Give the preparation type.
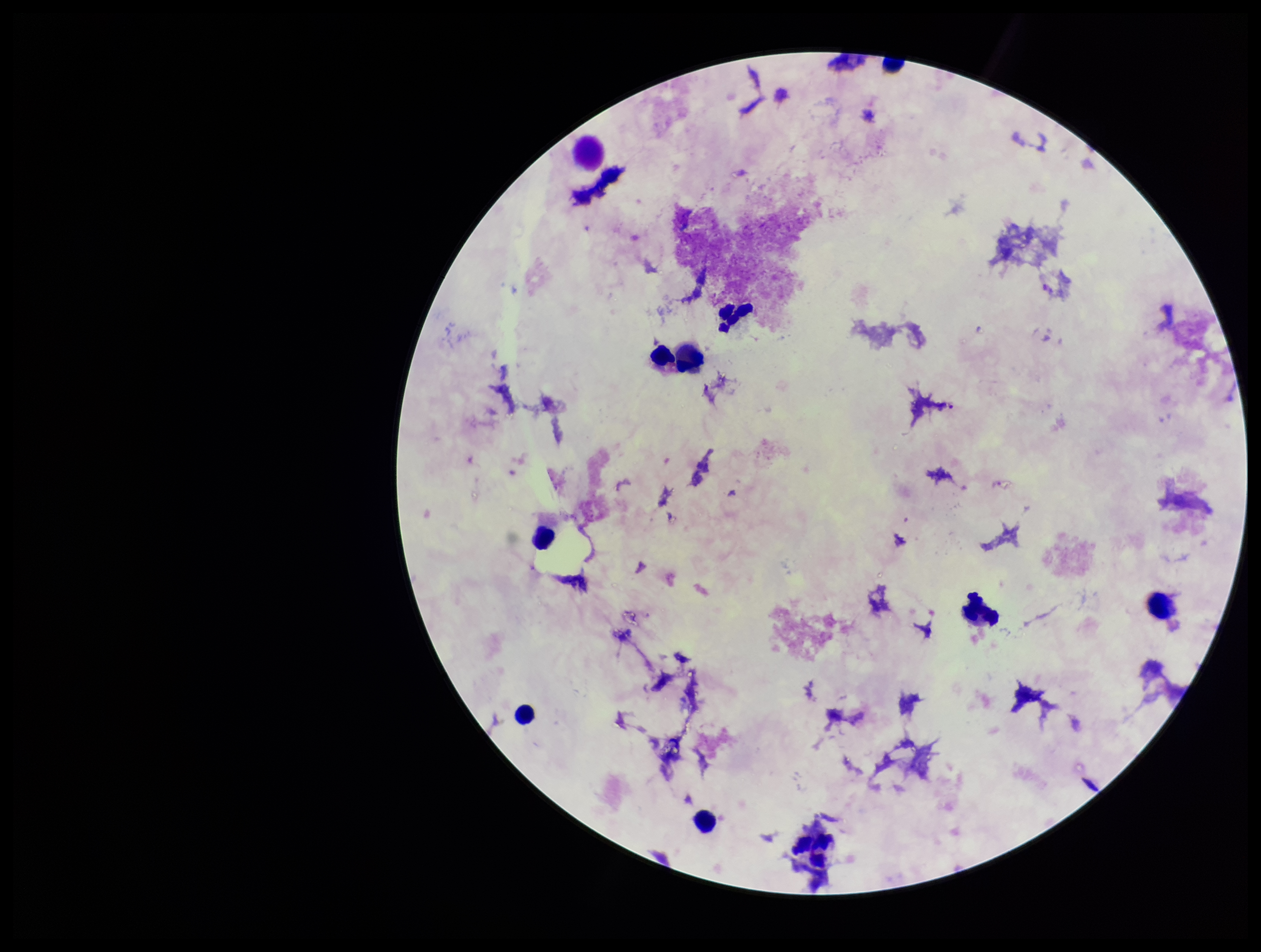
It is a thick blood smear.

Stained with Giemsa. Single field of view. Patient malaria status: negative. Smartphone photograph taken through the eyepiece of a microscope. Leukocyte count: 8. Plasmodium parasites: none identified. Image is 1261×952 pixels. Parasite count: 0.